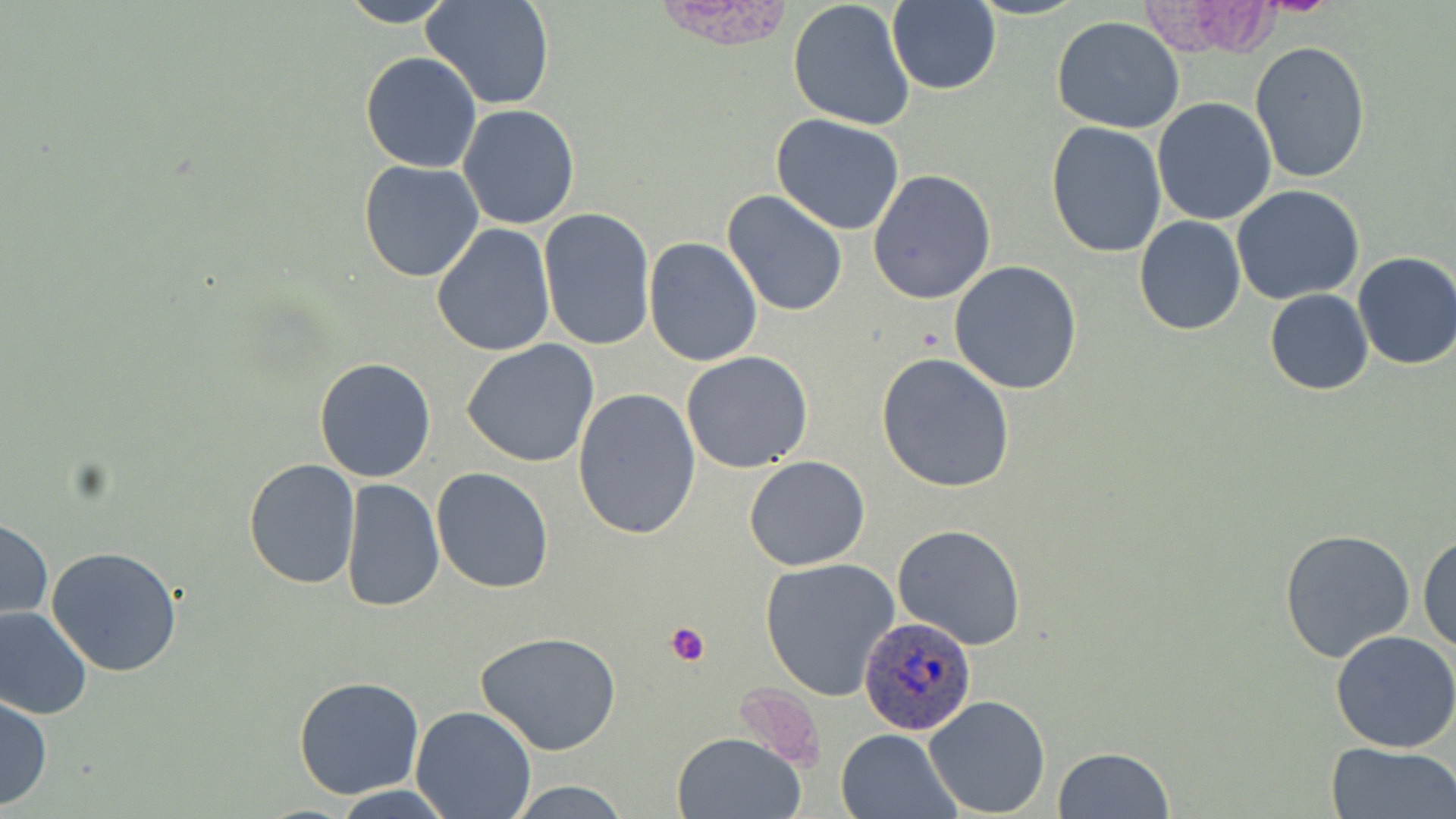
{
  "slide_level_diagnosis": "Plasmodium ovale",
  "preparation": "thin blood smear",
  "image_size": "1456×819 pixels",
  "modality": "optical microscopy",
  "uninfected_red_blood_cell_locations": "approximate bounding boxes as [x1, y1, x2, y2] in pixels: [333, 0, 459, 27], [422, 0, 554, 110], [787, 0, 916, 131], [969, 0, 1089, 20], [886, 1, 1000, 95], [1051, 17, 1186, 134], [1249, 41, 1372, 184], [360, 50, 484, 173], [1152, 96, 1276, 226], [456, 105, 580, 229], [770, 114, 905, 235], [1044, 121, 1168, 259], [358, 158, 486, 282], [868, 168, 997, 304], [1232, 185, 1365, 305], [722, 189, 850, 317], [536, 208, 656, 350], [1134, 216, 1246, 335], [431, 222, 557, 357], [642, 237, 763, 368], [1352, 251, 1456, 370], [948, 261, 1082, 395], [1265, 289, 1373, 396], [461, 339, 603, 468], [681, 350, 814, 473], [876, 352, 1016, 492], [314, 356, 436, 483], [573, 388, 702, 541], [744, 455, 871, 570], [242, 459, 362, 590], [431, 466, 557, 594], [339, 478, 445, 612], [0, 518, 53, 623], [893, 524, 1025, 649], [1278, 528, 1419, 666], [1418, 533, 1456, 657], [44, 547, 185, 678], [759, 558, 903, 701], [0, 605, 93, 721], [1330, 628, 1456, 753], [477, 632, 623, 757], [293, 676, 424, 800], [923, 694, 1051, 817], [0, 696, 52, 811], [409, 705, 538, 818], [835, 728, 960, 818], [671, 731, 805, 818], [1324, 740, 1456, 819], [1051, 747, 1176, 819], [505, 780, 635, 817], [326, 786, 461, 818]",
  "plasmodium_ovale_infected_red_blood_cell_locations": "approximate bounding boxes as [x1, y1, x2, y2] in pixels: [857, 618, 978, 735]",
  "platelet_locations": "approximate bounding boxes as [x1, y1, x2, y2] in pixels: [665, 620, 712, 666]",
  "field_of_view": "one of a larger specimen",
  "magnification": "1000x",
  "stain": "May-Grünwald-Giemsa"
}